Identify the parasite.
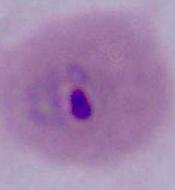
This is Plasmodium.

Summary:
  - Modality: micrograph
  - Magnification: 400x or 1000x